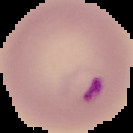
From a thin blood film. Image is 133×133 pixels. The area outside the segmented cell region is set to black. Result: Plasmodium parasites identified.